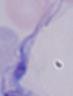
Summary:
  - Magnification: 1000x
  - Modality: photomicrograph
  - Identification: trypanosome